Assess for parasitized red blood cells.
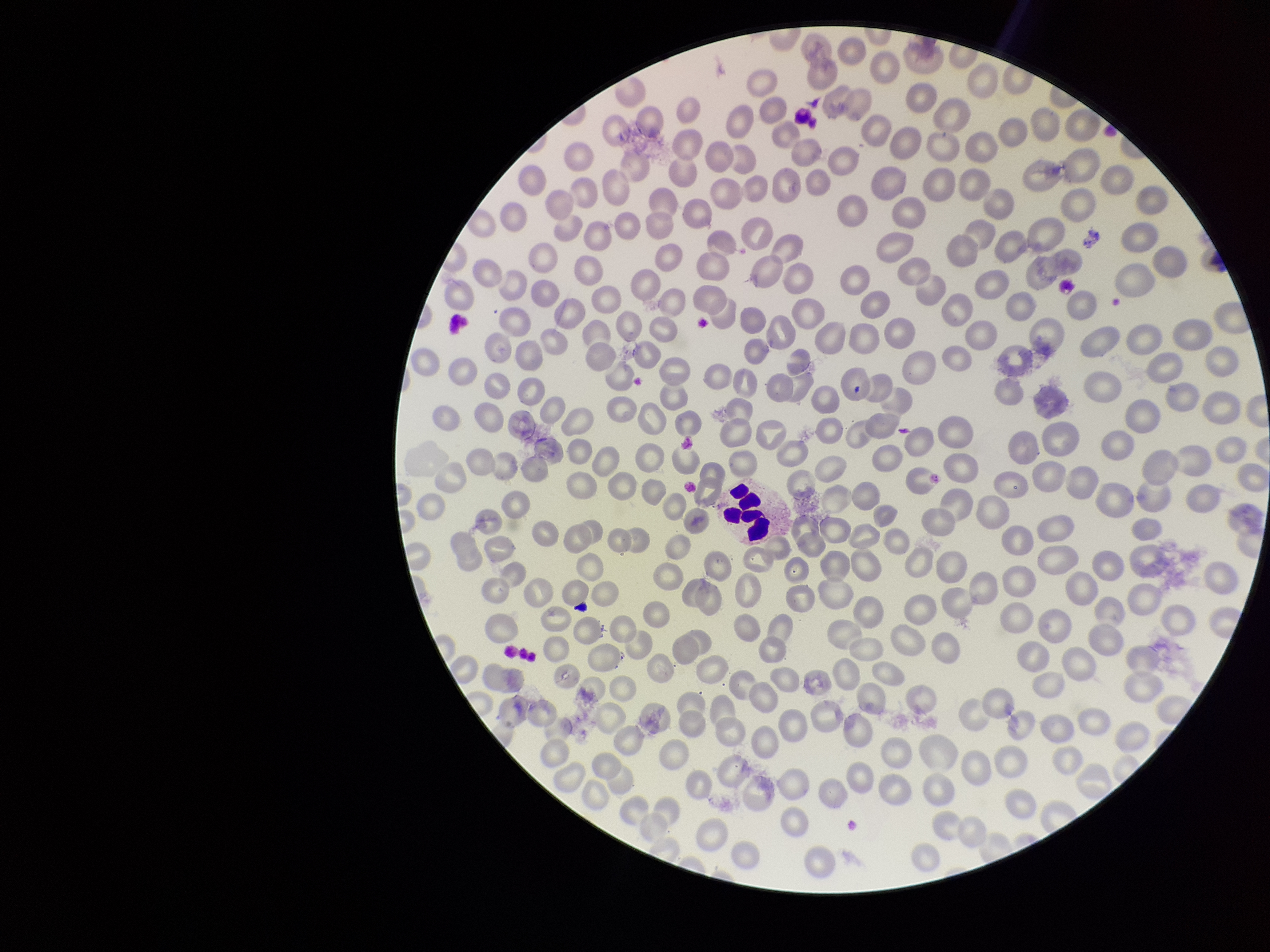

None detected.

Summary:
  - Image size: 1270×952 pixels
  - Field of view: single
  - Red blood cell count: 277
  - Preparation: thin
  - Patient malaria status: negative
  - Stain: Giemsa
  - Capture: smartphone photograph through the microscope eyepiece
  - Parasitized red blood cell count: 0